State which parasite is depicted.
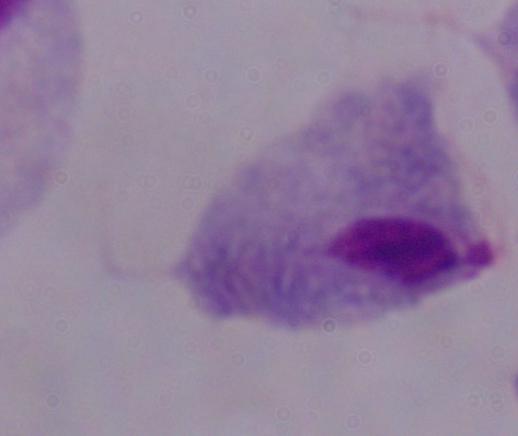

A trichomonad.

Summary:
  - Magnification: 1000x
  - Modality: photomicrograph